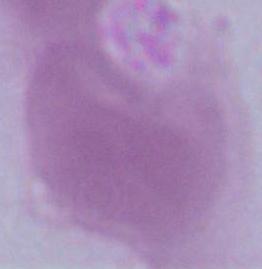

Micrograph. 1000x magnification. A red blood cell is shown.